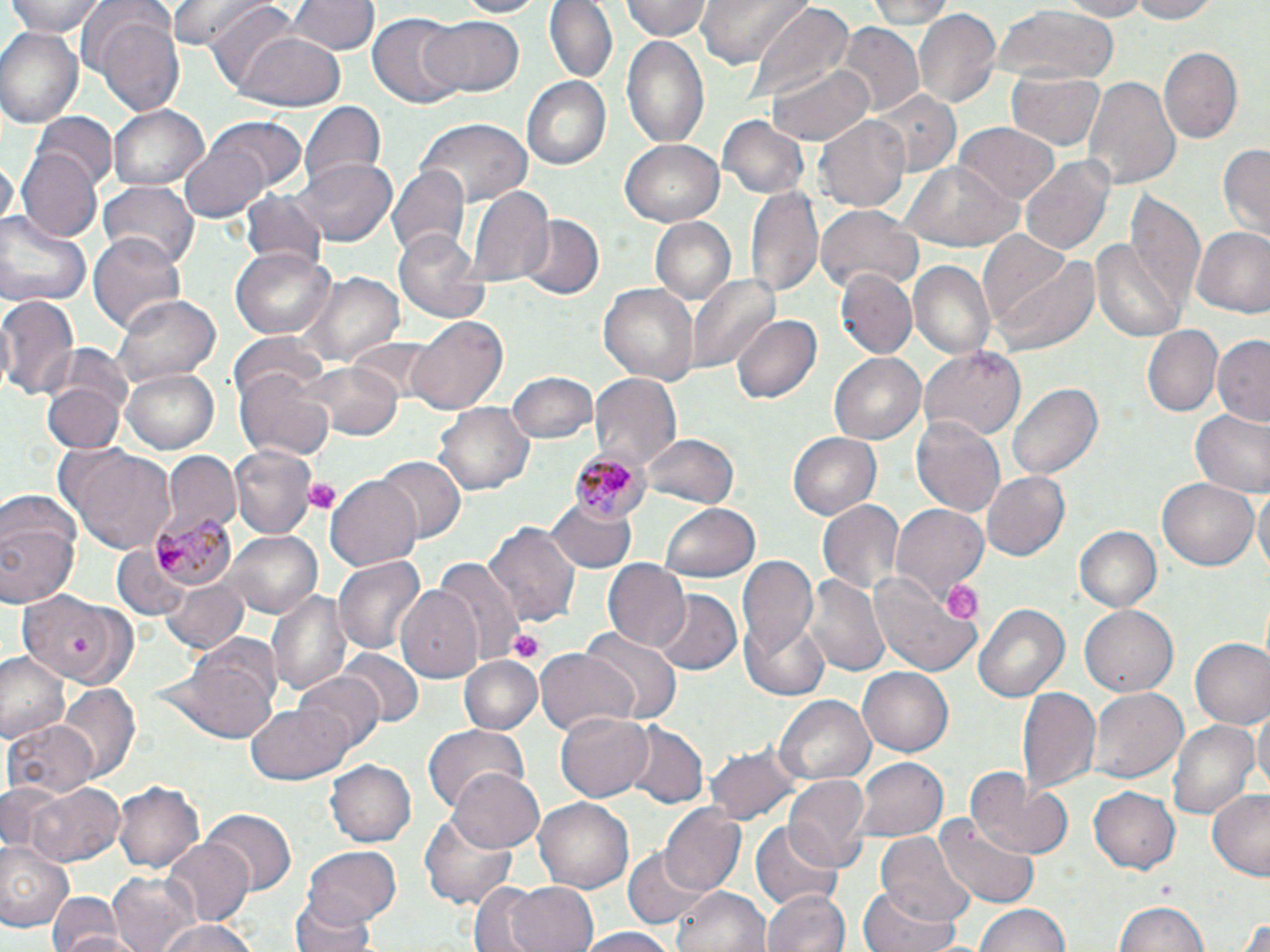
Approximate bounding boxes as named x1/y1/x2/y2 corners in pixels. Platelet locations: (x1=304, y1=476, x2=341, y2=514), (x1=940, y1=574, x2=986, y2=624), (x1=509, y1=629, x2=544, y2=663). Uninfected red blood cell locations: (x1=7, y1=0, x2=107, y2=39), (x1=167, y1=0, x2=275, y2=48), (x1=287, y1=0, x2=379, y2=56), (x1=451, y1=0, x2=549, y2=18), (x1=543, y1=0, x2=618, y2=86), (x1=619, y1=0, x2=712, y2=42), (x1=696, y1=0, x2=811, y2=70), (x1=1047, y1=0, x2=1158, y2=20), (x1=1124, y1=0, x2=1220, y2=24), (x1=863, y1=1, x2=961, y2=27), (x1=206, y1=3, x2=308, y2=97), (x1=747, y1=6, x2=854, y2=112), (x1=994, y1=7, x2=1118, y2=84), (x1=914, y1=8, x2=1001, y2=111), (x1=369, y1=12, x2=468, y2=111), (x1=91, y1=16, x2=185, y2=114), (x1=419, y1=16, x2=524, y2=96), (x1=835, y1=24, x2=923, y2=117), (x1=0, y1=26, x2=83, y2=129), (x1=237, y1=31, x2=347, y2=111), (x1=620, y1=34, x2=710, y2=150), (x1=1158, y1=47, x2=1241, y2=142), (x1=767, y1=60, x2=872, y2=146), (x1=1008, y1=71, x2=1106, y2=150), (x1=1084, y1=73, x2=1179, y2=190), (x1=519, y1=75, x2=611, y2=171), (x1=868, y1=89, x2=963, y2=177), (x1=300, y1=98, x2=384, y2=193), (x1=107, y1=105, x2=209, y2=190), (x1=31, y1=114, x2=115, y2=192), (x1=815, y1=115, x2=912, y2=214), (x1=210, y1=116, x2=307, y2=193), (x1=718, y1=117, x2=808, y2=199), (x1=420, y1=119, x2=533, y2=206), (x1=955, y1=122, x2=1059, y2=205), (x1=620, y1=139, x2=723, y2=225), (x1=179, y1=142, x2=270, y2=222), (x1=1218, y1=143, x2=1269, y2=239), (x1=16, y1=148, x2=102, y2=242), (x1=1019, y1=156, x2=1115, y2=256), (x1=1, y1=157, x2=16, y2=227), (x1=296, y1=157, x2=396, y2=245), (x1=900, y1=162, x2=1023, y2=250), (x1=387, y1=165, x2=469, y2=262), (x1=98, y1=179, x2=199, y2=267), (x1=747, y1=185, x2=823, y2=300), (x1=465, y1=188, x2=551, y2=284), (x1=239, y1=190, x2=327, y2=271), (x1=1127, y1=192, x2=1207, y2=313), (x1=816, y1=204, x2=923, y2=295), (x1=0, y1=211, x2=91, y2=307), (x1=518, y1=215, x2=603, y2=301), (x1=649, y1=218, x2=736, y2=307), (x1=1192, y1=226, x2=1270, y2=317), (x1=391, y1=227, x2=488, y2=322), (x1=90, y1=231, x2=185, y2=336), (x1=1092, y1=236, x2=1188, y2=343), (x1=987, y1=243, x2=1100, y2=358), (x1=232, y1=246, x2=336, y2=340), (x1=908, y1=260, x2=996, y2=358), (x1=838, y1=272, x2=917, y2=359), (x1=309, y1=274, x2=402, y2=366), (x1=689, y1=276, x2=782, y2=375), (x1=599, y1=284, x2=697, y2=383), (x1=113, y1=294, x2=220, y2=389), (x1=0, y1=295, x2=80, y2=400), (x1=732, y1=313, x2=820, y2=406), (x1=409, y1=316, x2=509, y2=414), (x1=1142, y1=325, x2=1222, y2=419), (x1=230, y1=334, x2=329, y2=411), (x1=1212, y1=335, x2=1269, y2=424), (x1=351, y1=338, x2=438, y2=404), (x1=918, y1=349, x2=1026, y2=443), (x1=829, y1=353, x2=926, y2=445), (x1=309, y1=363, x2=403, y2=441), (x1=120, y1=367, x2=220, y2=454), (x1=235, y1=367, x2=334, y2=461), (x1=45, y1=371, x2=130, y2=456), (x1=506, y1=371, x2=597, y2=443), (x1=589, y1=373, x2=681, y2=471), (x1=1007, y1=382, x2=1104, y2=479), (x1=434, y1=403, x2=534, y2=497), (x1=1190, y1=409, x2=1270, y2=498), (x1=912, y1=414, x2=1007, y2=516), (x1=642, y1=431, x2=738, y2=508), (x1=788, y1=431, x2=882, y2=522), (x1=62, y1=445, x2=180, y2=556), (x1=230, y1=447, x2=316, y2=536), (x1=161, y1=452, x2=240, y2=535), (x1=375, y1=457, x2=465, y2=544), (x1=980, y1=471, x2=1071, y2=562), (x1=326, y1=472, x2=423, y2=569), (x1=1156, y1=477, x2=1257, y2=570), (x1=1255, y1=486, x2=1269, y2=584), (x1=546, y1=491, x2=639, y2=573), (x1=1, y1=497, x2=83, y2=613), (x1=818, y1=499, x2=906, y2=599), (x1=661, y1=504, x2=759, y2=582), (x1=893, y1=505, x2=990, y2=603), (x1=484, y1=519, x2=580, y2=628), (x1=1074, y1=526, x2=1161, y2=613), (x1=222, y1=530, x2=323, y2=618), (x1=113, y1=545, x2=193, y2=620), (x1=737, y1=553, x2=820, y2=676), (x1=334, y1=556, x2=427, y2=655), (x1=432, y1=558, x2=525, y2=662), (x1=603, y1=560, x2=690, y2=651), (x1=867, y1=570, x2=982, y2=680), (x1=806, y1=574, x2=890, y2=679), (x1=159, y1=578, x2=248, y2=652), (x1=395, y1=586, x2=483, y2=683), (x1=267, y1=588, x2=354, y2=701), (x1=650, y1=590, x2=742, y2=676), (x1=17, y1=592, x2=129, y2=683), (x1=973, y1=603, x2=1070, y2=701), (x1=1081, y1=607, x2=1177, y2=695), (x1=739, y1=614, x2=831, y2=702), (x1=580, y1=630, x2=681, y2=724), (x1=1190, y1=638, x2=1270, y2=728), (x1=176, y1=645, x2=281, y2=744), (x1=536, y1=647, x2=638, y2=737), (x1=339, y1=649, x2=424, y2=730), (x1=0, y1=650, x2=69, y2=743), (x1=461, y1=654, x2=540, y2=732), (x1=859, y1=669, x2=953, y2=755), (x1=295, y1=670, x2=386, y2=752), (x1=57, y1=687, x2=141, y2=784), (x1=1018, y1=687, x2=1100, y2=800), (x1=1090, y1=688, x2=1186, y2=785), (x1=773, y1=695, x2=876, y2=787), (x1=1252, y1=702, x2=1270, y2=793), (x1=246, y1=705, x2=353, y2=784), (x1=555, y1=709, x2=655, y2=802), (x1=5, y1=718, x2=98, y2=800), (x1=1168, y1=720, x2=1258, y2=823), (x1=422, y1=723, x2=530, y2=813), (x1=621, y1=723, x2=706, y2=808), (x1=708, y1=746, x2=797, y2=820), (x1=854, y1=758, x2=946, y2=842), (x1=326, y1=760, x2=417, y2=848), (x1=449, y1=767, x2=547, y2=852), (x1=968, y1=769, x2=1075, y2=860), (x1=784, y1=775, x2=869, y2=869), (x1=114, y1=779, x2=205, y2=873), (x1=26, y1=781, x2=122, y2=867), (x1=0, y1=784, x2=62, y2=853), (x1=1090, y1=786, x2=1180, y2=873), (x1=1206, y1=789, x2=1270, y2=880), (x1=533, y1=796, x2=634, y2=893), (x1=659, y1=806, x2=747, y2=896), (x1=202, y1=810, x2=295, y2=896), (x1=420, y1=817, x2=516, y2=906), (x1=935, y1=818, x2=1040, y2=908), (x1=751, y1=819, x2=843, y2=911), (x1=876, y1=832, x2=975, y2=927), (x1=161, y1=835, x2=252, y2=926), (x1=1, y1=844, x2=70, y2=928), (x1=620, y1=844, x2=715, y2=928), (x1=302, y1=845, x2=402, y2=928), (x1=107, y1=871, x2=200, y2=952), (x1=462, y1=880, x2=554, y2=952), (x1=505, y1=882, x2=599, y2=952), (x1=857, y1=885, x2=962, y2=952), (x1=672, y1=886, x2=769, y2=952), (x1=291, y1=889, x2=380, y2=952), (x1=764, y1=889, x2=848, y2=952), (x1=47, y1=890, x2=125, y2=952), (x1=1115, y1=899, x2=1209, y2=952), (x1=975, y1=902, x2=1073, y2=952), (x1=1233, y1=913, x2=1270, y2=952), (x1=154, y1=917, x2=258, y2=952), (x1=575, y1=928, x2=681, y2=952), (x1=51, y1=929, x2=153, y2=952). Plasmodium malariae-infected red blood cell locations: (x1=570, y1=453, x2=648, y2=524), (x1=151, y1=511, x2=235, y2=583). Slide-level diagnosis: Plasmodium malariae. Captured at 1000x magnification. May-Grünwald-Giemsa-stained preparation. Single field of view. Thin blood smear. Image is 1270×952 pixels. Optical microscopy.